Locate and identify every blood parasite.
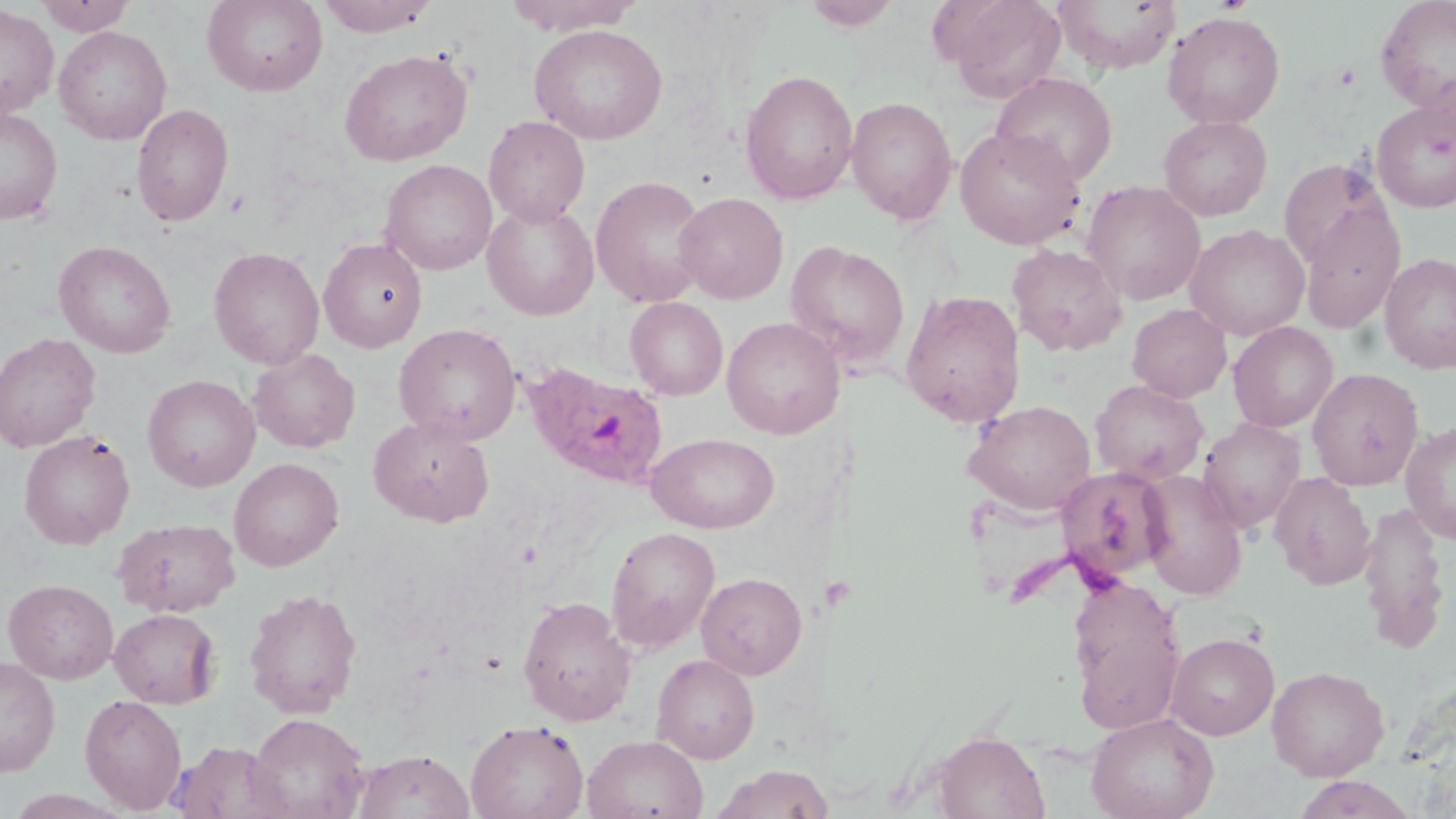

Approximate bounding boxes as (x1,y1)-(x2,y2) corner pairs in pixels.
Plasmodium ovale-infected red blood cells: (525,363)-(669,489).
No Plasmodium falciparum, Plasmodium malariae, Plasmodium vivax, Babesia divergens, or Trypanosoma brucei observed.

Summary:
  - Platelet locations: (829,574)-(857,614)
  - Uninfected red blood cell locations: (35,0)-(136,36), (202,0)-(328,97), (315,0)-(442,36), (503,0)-(644,36), (938,0)-(1067,103), (1053,0)-(1182,74), (1375,0)-(1456,118), (803,1)-(903,32), (0,4)-(59,121), (1162,10)-(1286,129), (529,24)-(667,144), (53,25)-(172,144), (339,48)-(472,167), (739,68)-(858,205), (991,73)-(1118,186), (845,95)-(958,225), (1371,98)-(1456,213), (132,104)-(234,227), (0,106)-(62,225), (483,115)-(590,227), (1158,115)-(1273,221), (954,126)-(1086,250), (1279,158)-(1393,272), (380,159)-(497,276), (590,175)-(710,308), (1083,180)-(1206,306), (674,192)-(788,304), (482,199)-(600,320), (1297,199)-(1406,334), (1186,225)-(1309,341), (319,238)-(427,353), (53,240)-(176,358), (785,240)-(910,368), (1007,244)-(1127,357), (208,246)-(325,369), (1379,252)-(1456,375), (901,289)-(1025,428), (626,297)-(728,401), (1127,303)-(1232,402), (721,317)-(845,439), (1228,321)-(1338,432), (393,323)-(522,445), (0,333)-(100,452), (248,349)-(360,453), (1308,368)-(1424,490), (142,374)-(260,492), (1090,380)-(1209,484), (964,400)-(1096,515), (368,415)-(495,527), (1198,417)-(1306,533), (1401,422)-(1456,543), (19,430)-(135,550), (646,432)-(779,534), (229,457)-(344,571), (1056,466)-(1175,582), (1136,470)-(1249,600), (1269,472)-(1376,590), (1358,501)-(1450,654), (113,518)-(240,617), (605,526)-(721,653), (696,572)-(807,680), (1066,575)-(1186,734), (3,579)-(119,684), (243,588)-(362,718), (517,595)-(637,726), (109,608)-(221,708), (1166,632)-(1279,740), (652,653)-(760,764), (0,656)-(60,777), (1267,665)-(1389,781), (79,694)-(187,813), (1085,712)-(1219,819), (246,713)-(370,819), (466,719)-(588,819), (932,730)-(1049,819), (582,734)-(708,819), (169,741)-(291,819), (353,749)-(474,819), (710,763)-(829,819), (1291,774)-(1417,819)
  - Slide-level diagnosis: Plasmodium ovale
  - Stain: May-Grünwald-Giemsa
  - Preparation: thin blood smear
  - Magnification: 1000x
  - Modality: light microscopy
  - Field of view: single
  - Image size: 1456×819 pixels